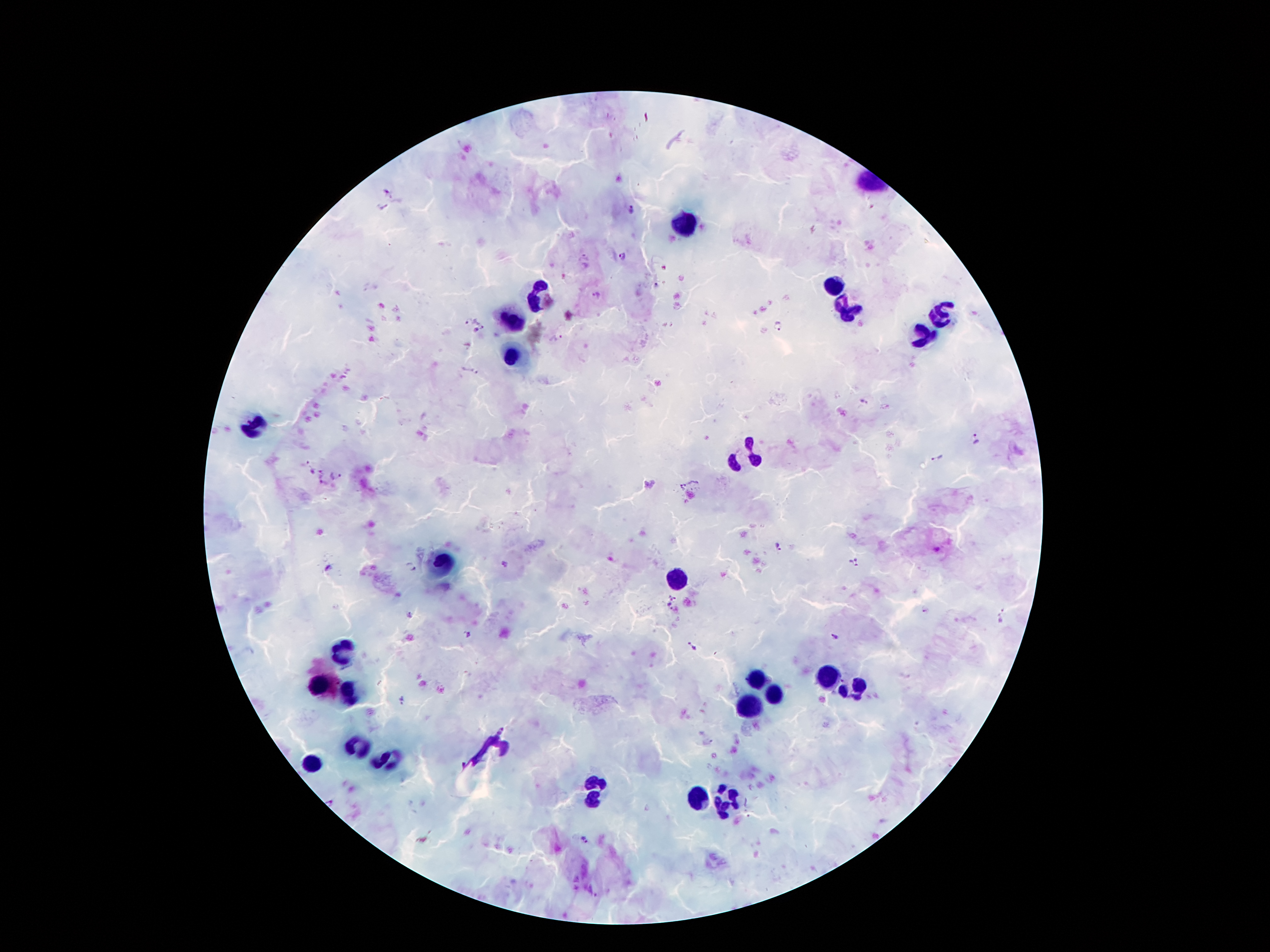
Approximate centers as [x, y] in pixels.
Summary:
  - Leukocyte locations: [677, 223], [837, 287], [536, 292], [850, 312], [941, 317], [513, 322], [923, 340], [514, 358], [251, 424], [747, 458], [445, 562], [676, 578], [340, 653], [828, 676], [757, 681], [321, 687], [853, 690], [346, 691], [773, 694], [750, 704], [356, 744], [491, 746], [388, 760], [308, 761], [595, 791], [701, 795], [726, 799]
  - Malaria parasite locations: [389, 190], [382, 207], [630, 211], [621, 257], [656, 285], [597, 294], [468, 320], [780, 326], [483, 327], [474, 331], [556, 336], [860, 401], [976, 438], [938, 458], [323, 469], [312, 470], [336, 475], [323, 484], [779, 547], [854, 562], [503, 564], [411, 567], [329, 569], [673, 597], [667, 609], [926, 610], [410, 614], [466, 633], [834, 636], [692, 646], [401, 697], [502, 729], [584, 839]
  - Image size: 1270×952 pixels
  - Patient malaria status: positive for Plasmodium falciparum
  - Preparation: thick blood film
  - Stain: Giemsa
  - Magnification: 100x
  - Capture: smartphone camera through the microscope eyepiece
  - Field of view: single